Assess this cell for malaria.
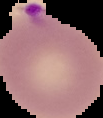
Parasitized.

Image is 103×118 pixels. From a thin blood smear. Segmented cell region on a black background.